Point out every Plasmodium parasite and every leukocyte.
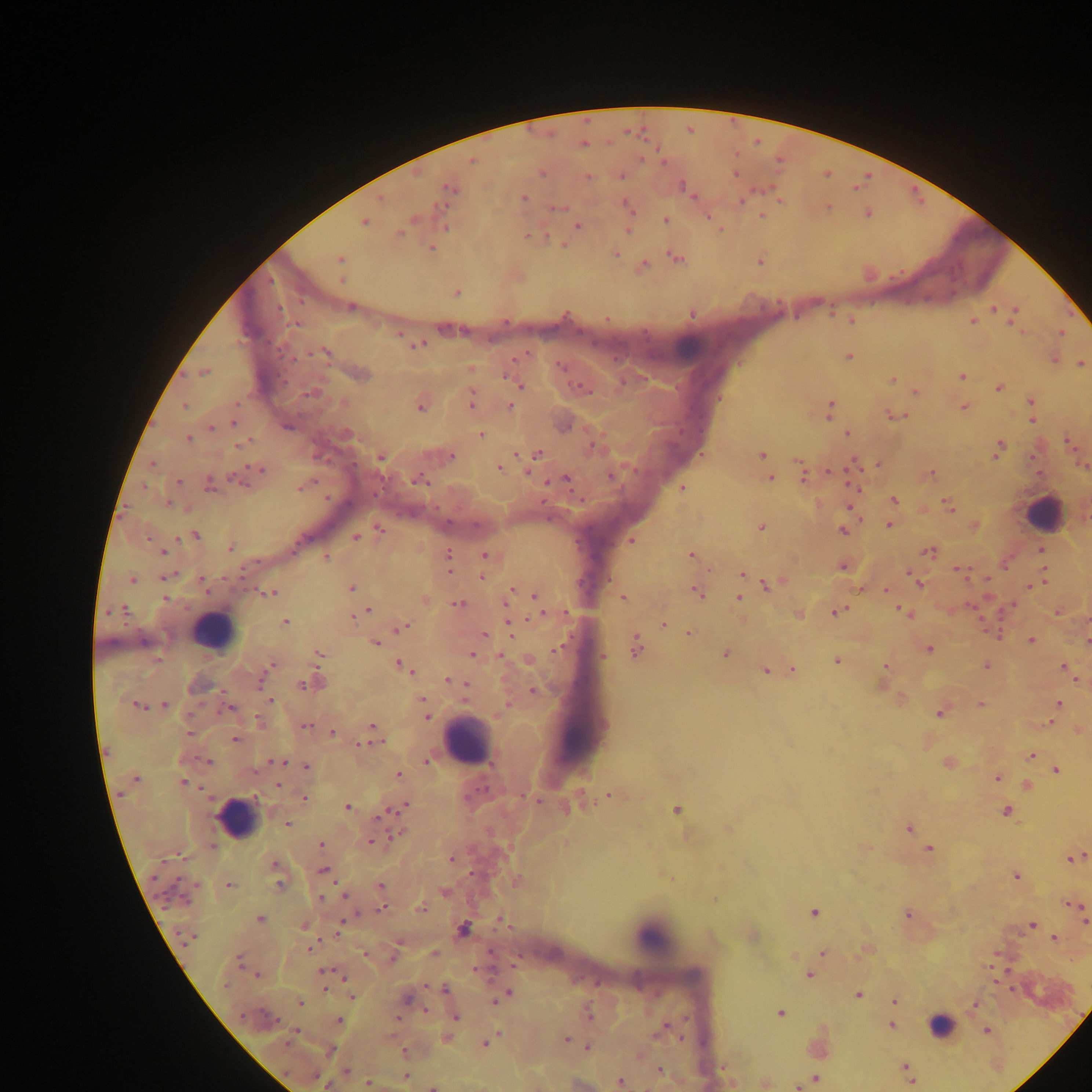

Approximate centers as [x, y] in pixels.
Plasmodium parasites: [583, 144], [472, 161], [542, 172], [736, 173], [588, 177], [622, 177], [450, 189], [684, 189], [524, 197], [626, 204], [828, 206], [556, 209], [867, 213], [762, 216], [665, 219], [364, 222], [577, 226], [446, 227], [628, 230], [399, 232], [431, 248], [616, 254], [340, 258], [676, 258], [760, 261], [644, 265], [342, 279], [456, 293], [351, 307], [994, 309], [1014, 312], [692, 314], [1012, 319], [972, 321], [1060, 333], [399, 335], [417, 345], [323, 353], [849, 356], [1055, 360], [1082, 364], [205, 372], [361, 374], [962, 376], [892, 380], [519, 385], [581, 388], [999, 388], [311, 392], [915, 392], [471, 401], [1031, 401], [344, 402], [184, 406], [511, 406], [420, 407], [964, 407], [830, 408], [897, 416], [1033, 420], [233, 422], [288, 427], [211, 428], [347, 433], [847, 433], [480, 435], [188, 438], [241, 444], [592, 446], [998, 448], [538, 453], [762, 455], [452, 456], [381, 457], [153, 464], [877, 464], [499, 468], [260, 470], [527, 471], [803, 473], [931, 474], [611, 477], [770, 478], [565, 479], [237, 481], [420, 482], [178, 483], [210, 484], [301, 487], [683, 489], [894, 500], [168, 504], [948, 505], [890, 525], [761, 527], [379, 529], [843, 531], [195, 536], [355, 538], [148, 539], [631, 540], [230, 548], [1040, 550], [163, 552], [928, 552], [691, 554], [485, 555], [448, 556], [327, 558], [842, 567], [962, 572], [742, 573], [482, 576], [164, 578], [132, 579], [202, 580], [916, 581], [1037, 584], [768, 585], [1032, 586], [352, 588], [512, 590], [886, 590], [696, 592], [272, 593], [535, 595], [623, 598], [740, 598], [166, 599], [425, 600], [459, 604], [124, 609], [369, 610], [902, 611], [838, 612], [360, 614], [541, 615], [352, 616], [285, 622], [664, 624], [509, 625], [403, 627], [688, 633], [483, 634], [1031, 641], [1087, 641], [375, 643], [636, 647], [558, 649], [929, 649], [320, 654], [472, 654], [726, 654], [500, 656], [602, 656], [837, 660], [272, 664], [401, 666], [886, 666], [986, 666], [1063, 667], [765, 670], [793, 670], [447, 680], [314, 683], [302, 684], [466, 684], [533, 691], [271, 701], [1058, 703], [164, 704], [980, 704], [137, 705], [229, 708], [939, 713], [426, 716], [258, 720], [305, 725], [372, 725], [332, 732], [189, 733], [235, 739], [363, 744], [1031, 755], [209, 762], [279, 762], [427, 762], [949, 763], [306, 766], [255, 770], [1056, 770], [399, 775], [997, 778], [135, 779], [183, 782], [278, 785], [1028, 785], [610, 795], [304, 798], [535, 800], [347, 806], [405, 806], [676, 809], [1006, 811], [390, 812], [383, 814], [287, 824], [908, 828], [397, 835], [373, 841], [320, 845], [213, 846], [929, 849], [452, 858], [1074, 858], [275, 864], [324, 870], [1016, 876], [280, 885], [229, 886], [381, 886], [344, 895], [321, 898], [1076, 906], [421, 908], [382, 909], [814, 912], [907, 914], [260, 919], [1084, 919], [1032, 925], [304, 926], [338, 928], [463, 930], [190, 937], [1055, 939], [309, 948], [823, 953], [434, 954], [364, 955], [239, 958], [325, 972], [258, 975], [809, 975], [226, 984], [324, 989], [445, 990], [858, 995], [352, 997], [502, 997], [407, 999], [496, 1000], [895, 1001], [300, 1003], [974, 1005], [427, 1011], [780, 1013], [589, 1016], [455, 1017], [339, 1020], [891, 1025], [664, 1028], [987, 1031], [296, 1032], [291, 1037], [446, 1038], [566, 1038], [485, 1043], [587, 1048], [328, 1051], [405, 1052], [905, 1066], [346, 1071], [660, 1071], [908, 1072], [405, 1077], [815, 1079], [911, 1080], [368, 1082], [620, 1082], [327, 1085], [433, 1087].
Leukocytes: [688, 347], [1042, 511], [215, 632], [466, 742], [236, 818], [654, 937], [938, 1025].

capture = mobile-phone photograph through a microscope
country = Ghana
preparation = thick blood film
image size = 1092×1092 pixels
field of view = single